Classify this cell by malaria status.
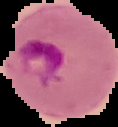

It is parasitized.

image size = 118×127 pixels
image type = segmented cell region on a black background
preparation = thin blood smear